Comment on the morphology of the red blood cells.
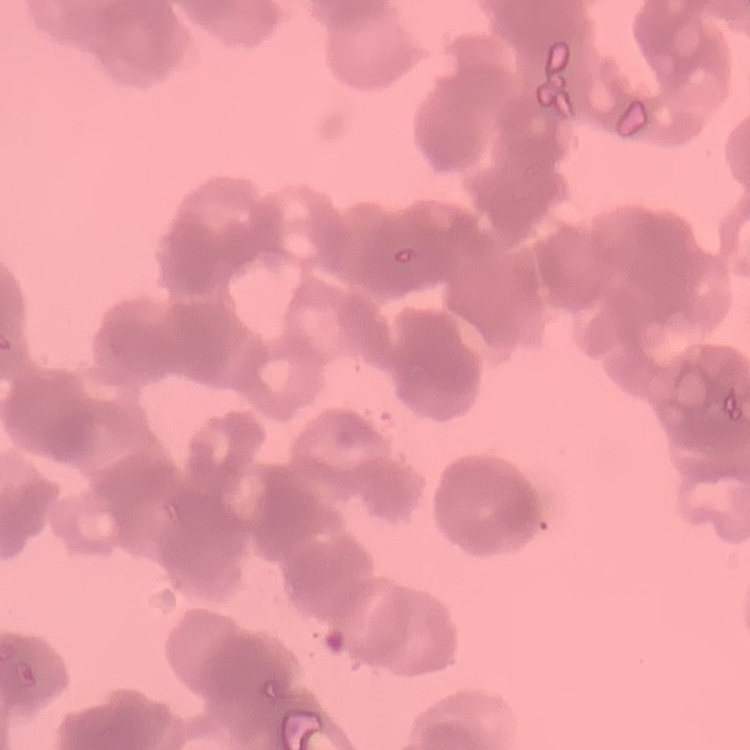

Rouleaux formation.

preparation = thin blood smear
stain = Field's or Giemsa
image type = square crop of a larger photomicrograph